Locate and identify every blood parasite.
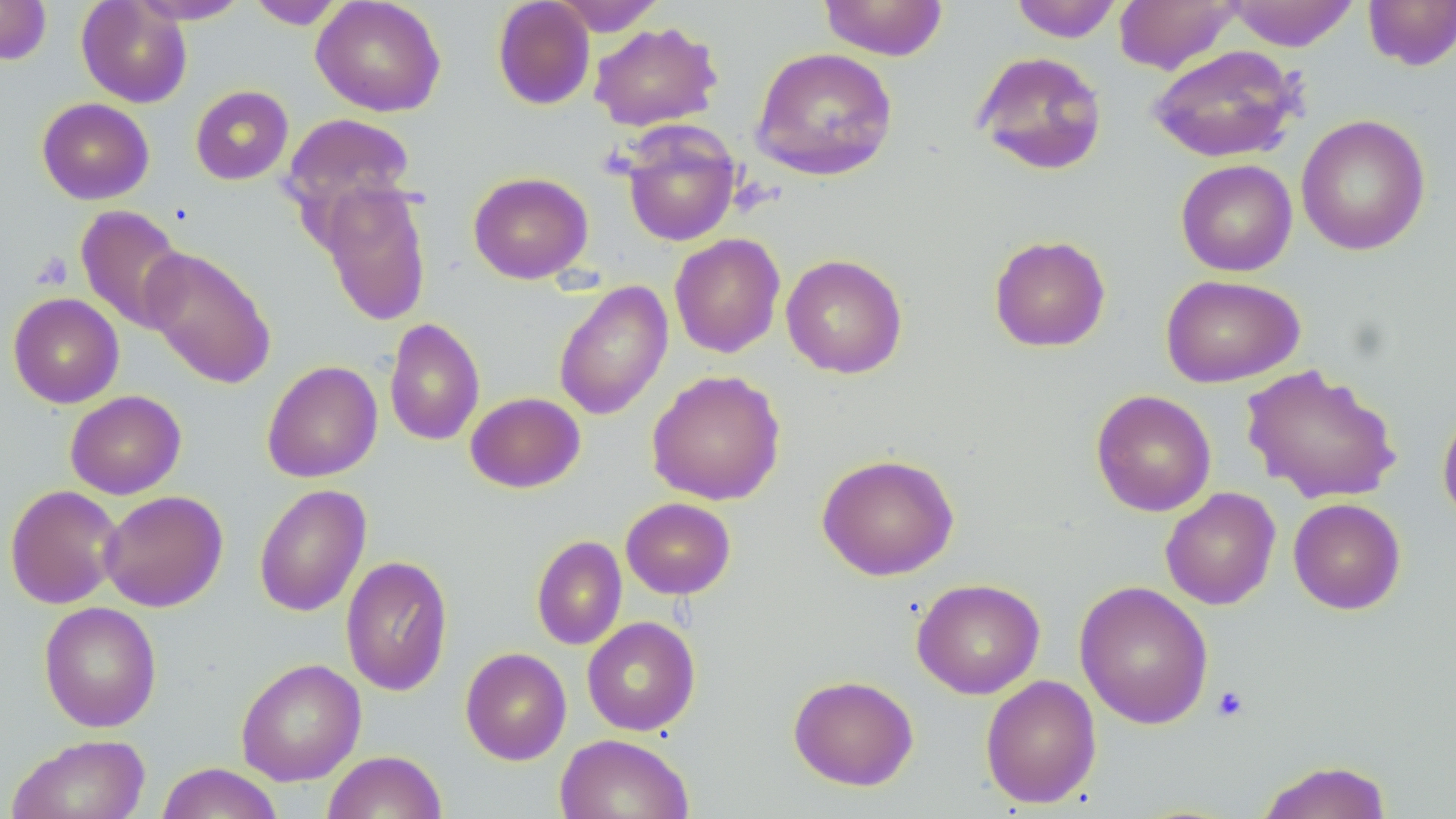

No blood parasites observed.

Summary:
  - Coordinate format: approximate bounding boxes as named x1/y1/x2/y2 corners in pixels
  - Uninfected red blood cell locations: (x1=0, y1=0, x2=52, y2=65), (x1=76, y1=0, x2=192, y2=108), (x1=130, y1=0, x2=250, y2=24), (x1=311, y1=0, x2=446, y2=117), (x1=492, y1=0, x2=596, y2=110), (x1=550, y1=0, x2=666, y2=35), (x1=819, y1=0, x2=949, y2=61), (x1=1009, y1=0, x2=1124, y2=42), (x1=1114, y1=0, x2=1242, y2=74), (x1=1224, y1=0, x2=1360, y2=51), (x1=1362, y1=0, x2=1456, y2=71), (x1=246, y1=1, x2=347, y2=29), (x1=589, y1=21, x2=722, y2=132), (x1=1147, y1=44, x2=1304, y2=164), (x1=750, y1=47, x2=898, y2=181), (x1=972, y1=51, x2=1108, y2=176), (x1=190, y1=85, x2=293, y2=185), (x1=37, y1=97, x2=154, y2=205), (x1=279, y1=112, x2=418, y2=227), (x1=1295, y1=114, x2=1431, y2=256), (x1=620, y1=123, x2=741, y2=246), (x1=1175, y1=159, x2=1297, y2=276), (x1=468, y1=171, x2=593, y2=284), (x1=318, y1=181, x2=433, y2=326), (x1=75, y1=205, x2=187, y2=333), (x1=669, y1=233, x2=785, y2=358), (x1=988, y1=235, x2=1111, y2=352), (x1=139, y1=246, x2=277, y2=389), (x1=781, y1=254, x2=908, y2=378), (x1=1161, y1=274, x2=1305, y2=388), (x1=553, y1=280, x2=673, y2=421), (x1=8, y1=293, x2=124, y2=408), (x1=383, y1=318, x2=485, y2=446), (x1=261, y1=360, x2=383, y2=483), (x1=1241, y1=363, x2=1401, y2=505), (x1=647, y1=369, x2=786, y2=505), (x1=1090, y1=389, x2=1217, y2=517), (x1=65, y1=390, x2=186, y2=499), (x1=465, y1=392, x2=585, y2=493), (x1=1437, y1=405, x2=1456, y2=526), (x1=816, y1=453, x2=959, y2=581), (x1=253, y1=483, x2=372, y2=617), (x1=5, y1=484, x2=124, y2=609), (x1=1160, y1=487, x2=1281, y2=609), (x1=99, y1=489, x2=228, y2=612), (x1=621, y1=497, x2=736, y2=599), (x1=1288, y1=497, x2=1406, y2=614), (x1=531, y1=535, x2=627, y2=650), (x1=340, y1=555, x2=453, y2=696), (x1=911, y1=578, x2=1046, y2=699), (x1=1074, y1=580, x2=1214, y2=729), (x1=39, y1=601, x2=162, y2=732), (x1=581, y1=616, x2=701, y2=735), (x1=460, y1=647, x2=571, y2=765), (x1=236, y1=658, x2=366, y2=786), (x1=788, y1=674, x2=919, y2=791), (x1=980, y1=674, x2=1102, y2=808), (x1=6, y1=733, x2=151, y2=819), (x1=554, y1=733, x2=693, y2=819), (x1=322, y1=750, x2=447, y2=819), (x1=1255, y1=760, x2=1393, y2=819), (x1=156, y1=763, x2=284, y2=818)
  - Platelet locations: (x1=32, y1=252, x2=74, y2=290), (x1=1211, y1=685, x2=1249, y2=722)
  - Slide-level diagnosis: negative for blood parasites
  - Magnification: 1000x
  - Image size: 1456×819 pixels
  - Preparation: thin blood film
  - Modality: optical microscopy
  - Field of view: one of a larger specimen
  - Stain: May-Grünwald-Giemsa